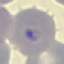 Result: malaria parasites detected. Acquired by smartphone through the microscope eyepiece. Cell patch, automatically extracted from a larger field of view and resized to 64 × 64 pixels. Thin blood film. Giemsa stain.